State which cell type is depicted.
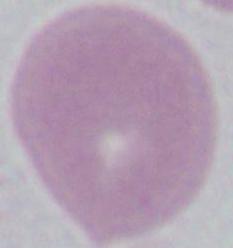
This is an erythrocyte.

Micrograph. 1000x magnification.